Look for Plasmodium parasites.
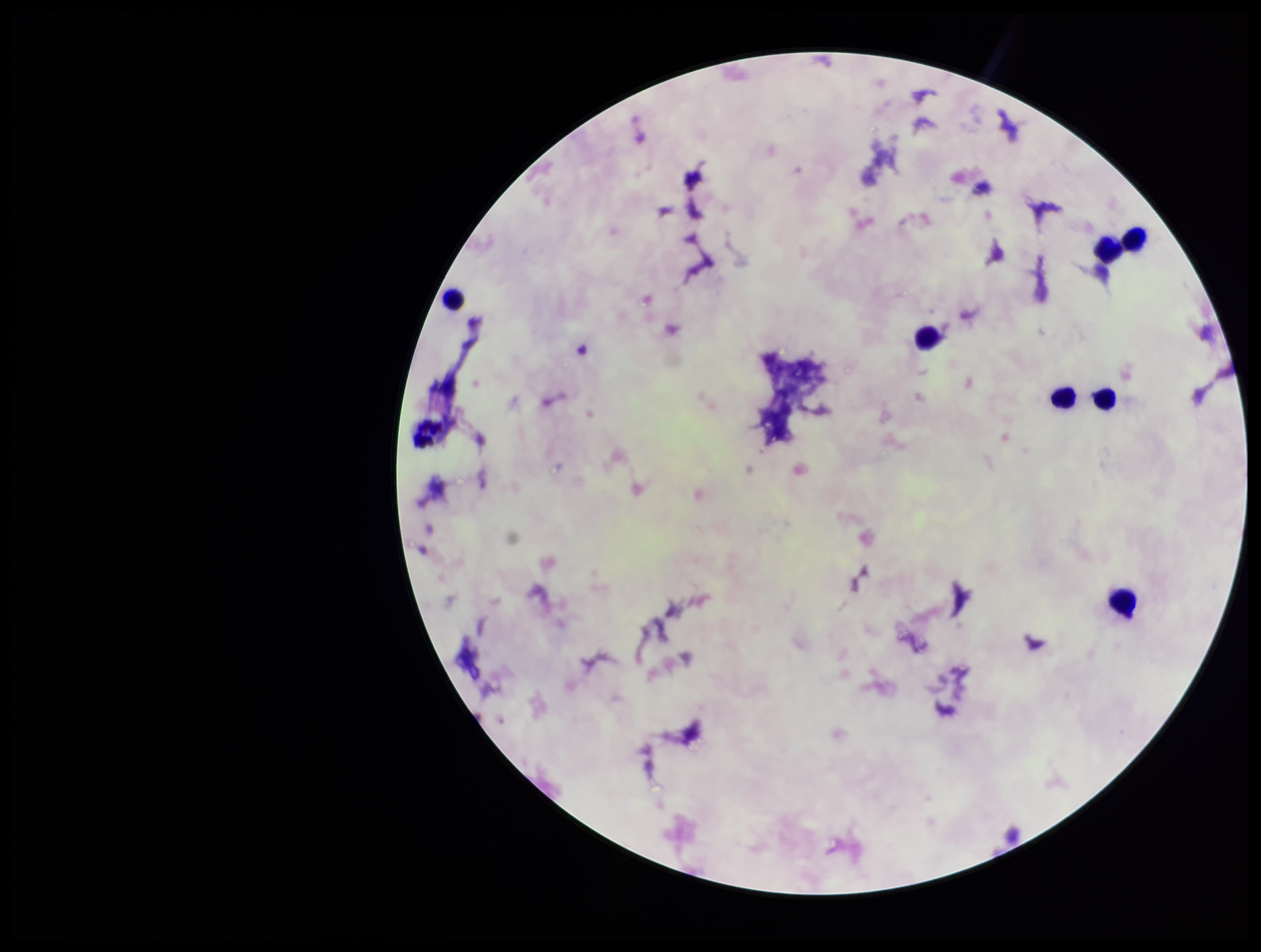
None detected.

Stained with Giemsa. Parasite count: 0. Patient malaria status: negative. Preparation: thick smear. Image is 1261×952 pixels. One field from this slide. Smartphone photograph taken through the eyepiece of a microscope. Leukocyte count: 8.